Assess for malaria.
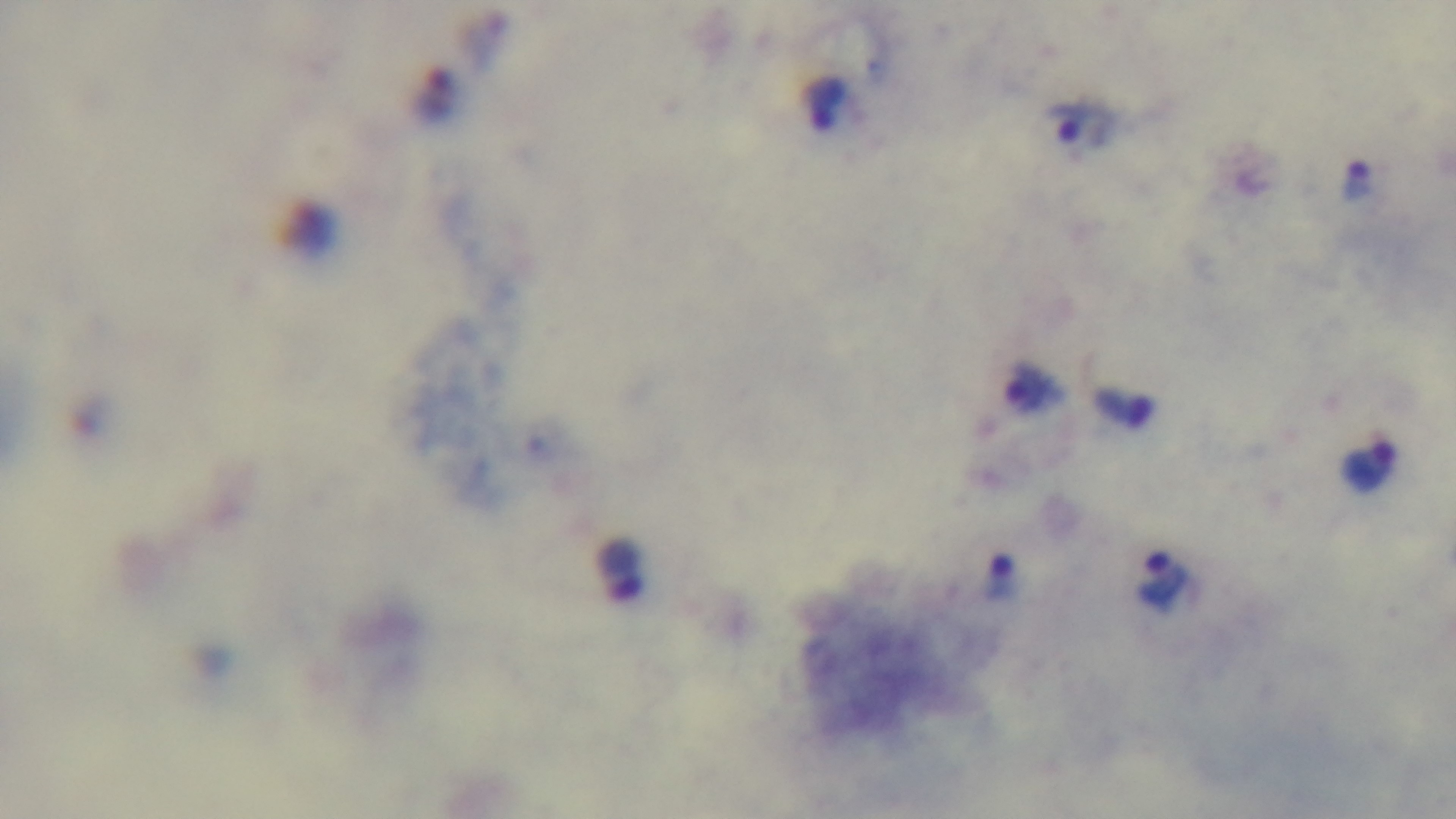
It is infected.

field of view = one from the slide
capture = mounted 4K digital camera
modality = light microscopy
stain = Giemsa
preparation = thick smear
objective = 100x oil immersion